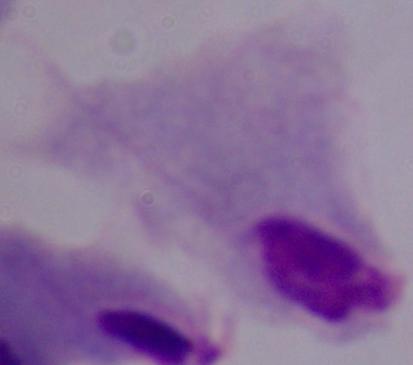
{
  "magnification": "1000x",
  "identification": "trichomonad",
  "modality": "photomicrograph"
}